Assess this cell for malaria.
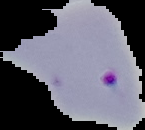
It is parasitized.

image_type: cell region segmented out of the field of view; surrounding area masked to black
image_size: 145×130 pixels
preparation: thin blood smear